Give the extent of all Plasmodium malariae-infected red blood cells.
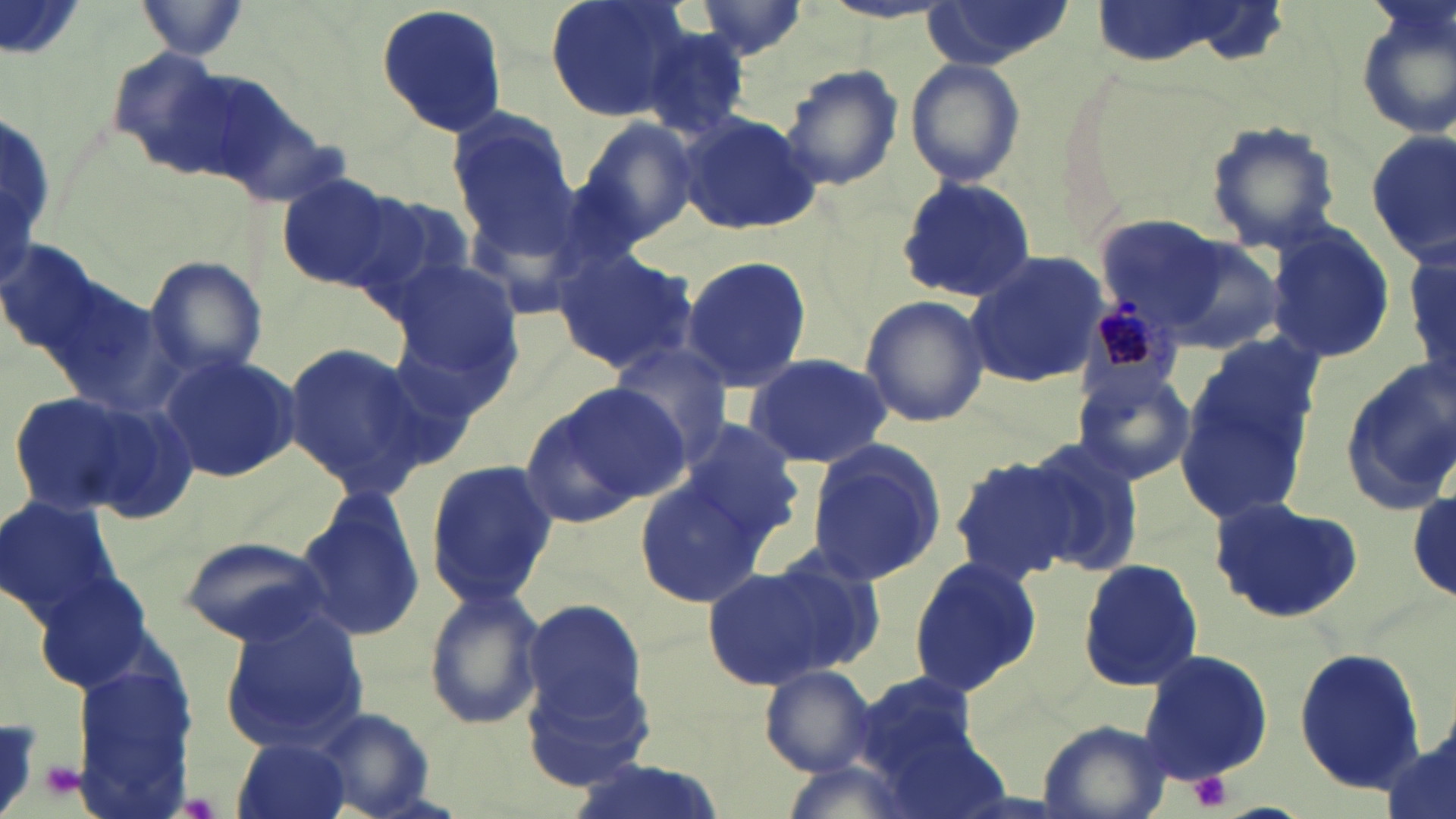

Approximate bounding boxes as named x1/y1/x2/y2 corners in pixels.
Plasmodium malariae-infected red blood cells: (x1=1082, y1=296, x2=1183, y2=403).

slide-level diagnosis = Plasmodium malariae
preparation = thin blood smear
stain = May-Grünwald-Giemsa
platelet locations = approximate bounding boxes as named x1/y1/x2/y2 corners in pixels: (x1=0, y1=718, x2=40, y2=814), (x1=41, y1=760, x2=84, y2=800), (x1=1189, y1=771, x2=1235, y2=811), (x1=176, y1=795, x2=220, y2=818)
image size = 1456×819 pixels
magnification = 1000x
uninfected red blood cell locations = approximate bounding boxes as named x1/y1/x2/y2 corners in pixels: (x1=134, y1=0, x2=252, y2=59), (x1=544, y1=0, x2=692, y2=122), (x1=690, y1=0, x2=811, y2=60), (x1=921, y1=1, x2=1070, y2=71), (x1=1351, y1=1, x2=1456, y2=142), (x1=373, y1=2, x2=511, y2=140), (x1=639, y1=28, x2=753, y2=141), (x1=904, y1=58, x2=1027, y2=187), (x1=780, y1=62, x2=904, y2=191), (x1=447, y1=109, x2=579, y2=245), (x1=678, y1=113, x2=823, y2=236), (x1=1203, y1=118, x2=1343, y2=255), (x1=577, y1=119, x2=699, y2=244), (x1=1364, y1=132, x2=1454, y2=265), (x1=278, y1=175, x2=403, y2=291), (x1=896, y1=176, x2=1037, y2=301), (x1=343, y1=193, x2=478, y2=310), (x1=1097, y1=218, x2=1231, y2=331), (x1=1268, y1=227, x2=1395, y2=362), (x1=1140, y1=231, x2=1290, y2=357), (x1=1406, y1=242, x2=1456, y2=392), (x1=551, y1=246, x2=700, y2=376), (x1=964, y1=250, x2=1104, y2=392), (x1=680, y1=255, x2=811, y2=392), (x1=146, y1=256, x2=269, y2=385), (x1=388, y1=257, x2=522, y2=381), (x1=857, y1=296, x2=990, y2=430), (x1=280, y1=340, x2=431, y2=496), (x1=609, y1=341, x2=735, y2=466), (x1=157, y1=352, x2=301, y2=483), (x1=744, y1=352, x2=893, y2=466), (x1=1173, y1=352, x2=1319, y2=524), (x1=1337, y1=363, x2=1456, y2=514), (x1=1072, y1=364, x2=1197, y2=486), (x1=520, y1=388, x2=677, y2=527), (x1=6, y1=390, x2=153, y2=520), (x1=676, y1=418, x2=805, y2=543), (x1=1020, y1=436, x2=1147, y2=574), (x1=804, y1=439, x2=950, y2=586), (x1=946, y1=454, x2=1079, y2=583), (x1=426, y1=460, x2=555, y2=609), (x1=635, y1=474, x2=766, y2=607), (x1=1408, y1=489, x2=1456, y2=602), (x1=295, y1=490, x2=425, y2=643), (x1=0, y1=496, x2=121, y2=621), (x1=1209, y1=498, x2=1361, y2=623), (x1=177, y1=533, x2=336, y2=646), (x1=906, y1=554, x2=1043, y2=699), (x1=1077, y1=559, x2=1205, y2=693), (x1=703, y1=560, x2=869, y2=691), (x1=421, y1=587, x2=548, y2=732), (x1=521, y1=599, x2=647, y2=725), (x1=217, y1=612, x2=370, y2=757), (x1=1135, y1=646, x2=1274, y2=788), (x1=1293, y1=647, x2=1426, y2=795), (x1=759, y1=665, x2=878, y2=776), (x1=522, y1=668, x2=659, y2=791), (x1=854, y1=672, x2=984, y2=778), (x1=310, y1=707, x2=440, y2=818), (x1=1034, y1=720, x2=1173, y2=819), (x1=1377, y1=733, x2=1454, y2=819), (x1=230, y1=738, x2=352, y2=819), (x1=568, y1=757, x2=723, y2=819)
field of view = one of a larger specimen
modality = optical microscopy